Assess this cell for malaria.
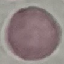

It is uninfected.

{
  "stain": "Giemsa",
  "capture": "smartphone through the microscope eyepiece",
  "preparation": "thin blood film",
  "image_type": "automatically extracted cell patch, resized to 64 × 64 pixels"
}